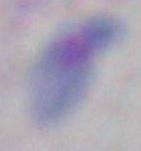
Summary:
  - Modality: micrograph
  - Magnification: 1000x
  - Identification: Toxoplasma gondii